Comment on the morphology of the red blood cells.
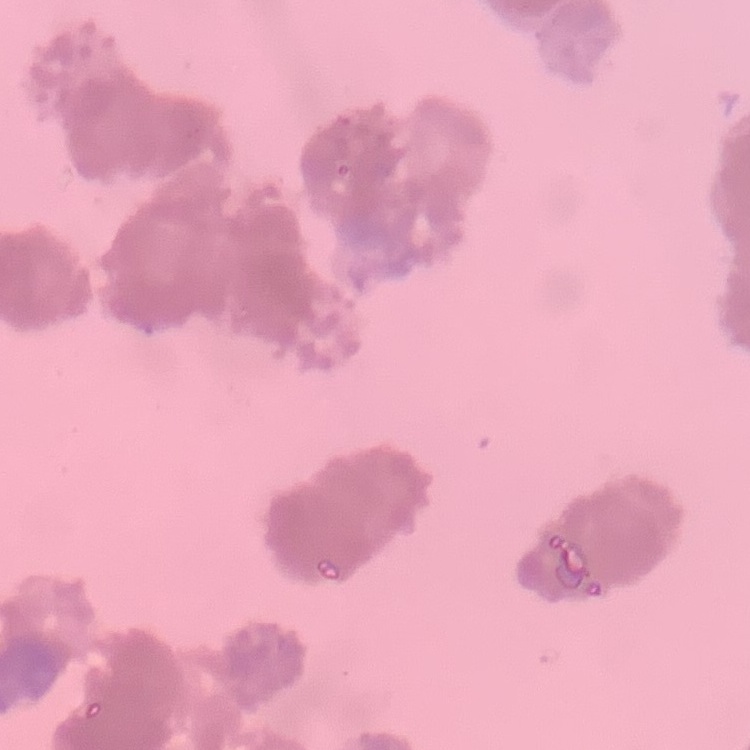
They show rouleaux formation.

Thin blood smear. Stained with either Field's or Giemsa. Square crop of a larger photomicrograph.